Identify the parasite.
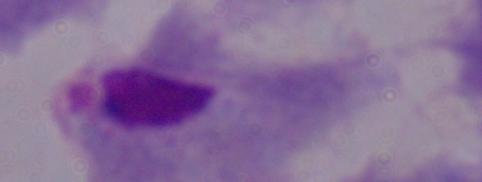
A trichomonad.

modality = micrograph
magnification = 1000x